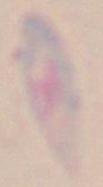 Micrograph. Toxoplasma gondii is seen. 1000x magnification.